Assess this cell for malaria.
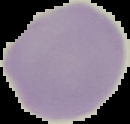
It is uninfected.

Image is 130×124 pixels. From a thin blood film. Segmented cell region on a black background.